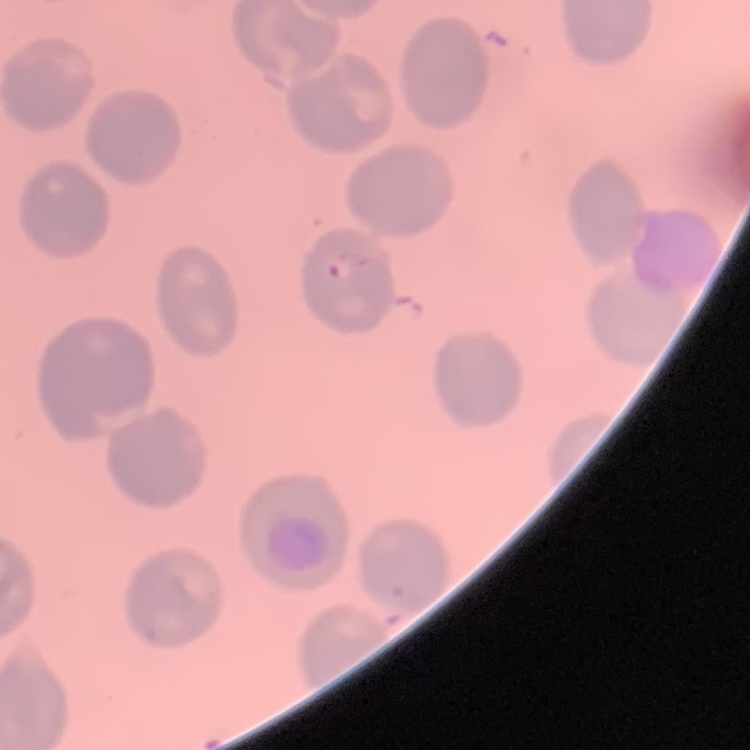
erythrocyte_morphology: no rouleaux formation
image_type: square crop of a larger photomicrograph
preparation: thin blood film
stain: Field's or Giemsa